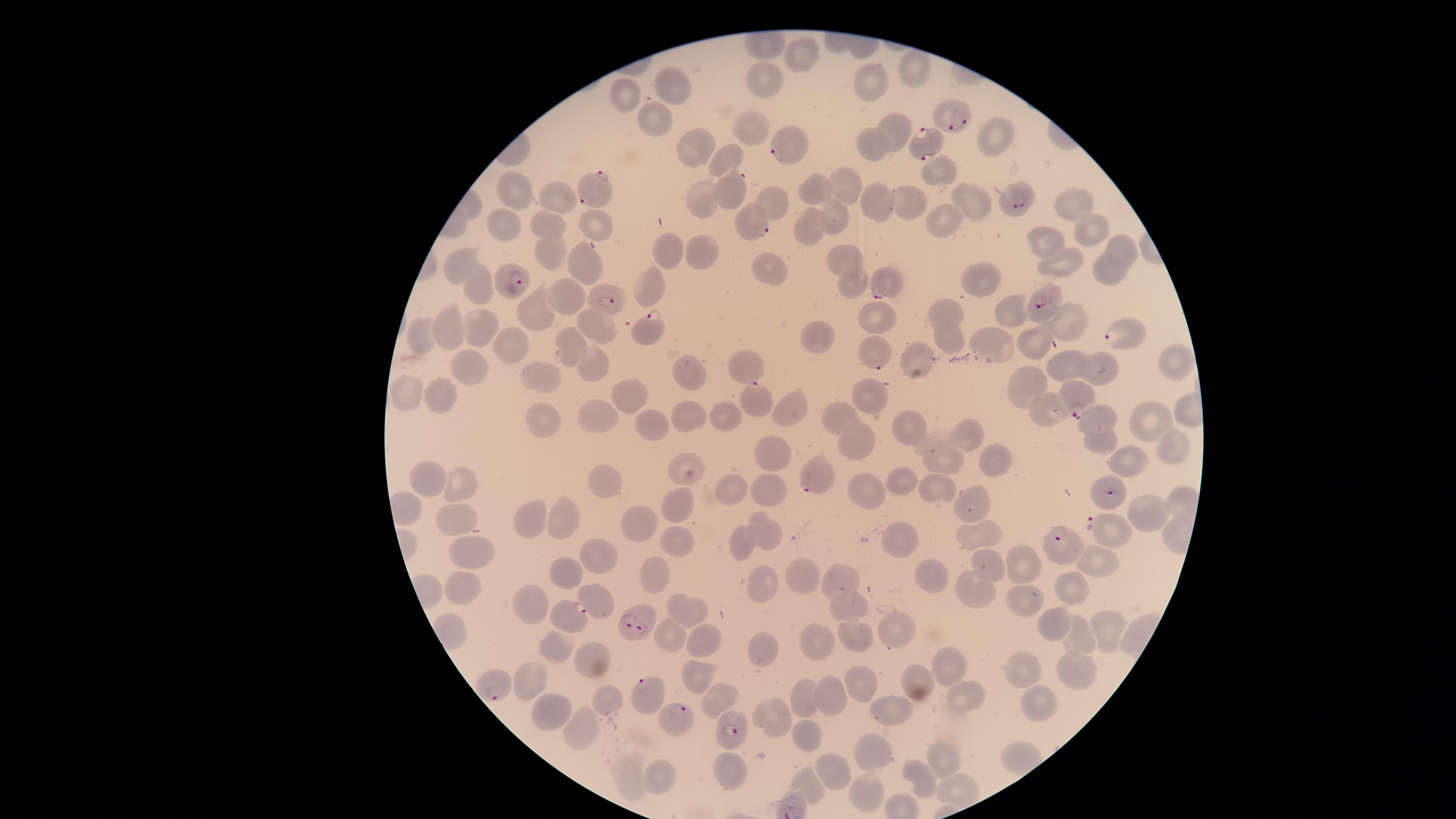
image_size: 1456×819 pixels
parasitized_RBCs: 'approximate marker points as (x, y) in pixels: (953, 122), (925, 144), (785, 148), (594, 190), (1019, 203), (756, 221), (517, 278), (886, 286), (606, 296), (1043, 306), (651, 328), (1120, 337), (877, 355), (755, 397), (1075, 398), (819, 476), (1114, 493), (1096, 525), (1061, 541), (570, 616), (642, 616), (487, 687), (644, 693), (679, 719), (728, 733)'
field_of_view: single
visible_region: circular
species: Plasmodium falciparum
stain: Giemsa
capture: smartphone photograph through the microscope eyepiece
presence: malaria parasites identified
uninfected_RBCs: 'approximate marker points as (x, y) in pixels: (805, 59), (910, 69), (873, 81), (764, 85), (673, 89), (620, 91), (650, 119), (749, 129), (894, 131), (997, 134), (872, 145), (691, 149), (730, 157), (938, 168), (843, 185), (518, 192), (817, 193), (732, 194), (557, 196), (1072, 199), (773, 200), (974, 200), (701, 201), (907, 202), (879, 207), (940, 216), (829, 218), (505, 224), (596, 224), (547, 226), (808, 228), (1082, 231), (1050, 238), (1118, 247), (697, 251), (666, 252), (553, 253), (841, 260), (585, 265), (463, 266), (1062, 267), (1112, 269), (776, 270), (976, 281), (855, 285), (478, 287), (652, 288), (571, 296), (944, 308), (1006, 310), (536, 311), (880, 320), (1069, 322), (478, 328), (440, 331), (593, 331), (820, 335), (947, 336), (421, 338), (1031, 339), (513, 343), (993, 344), (566, 346), (1171, 359), (917, 360), (749, 362), (591, 365), (1067, 365), (1101, 368), (696, 369), (466, 370), (542, 377), (1029, 383), (440, 394), (870, 394), (404, 395), (629, 398), (1048, 408), (791, 410), (723, 411), (1101, 411), (688, 412), (601, 415), (544, 417), (1143, 417), (841, 419), (659, 428), (912, 429), (851, 437), (967, 437), (932, 442), (1099, 445), (1172, 448), (773, 454), (943, 459), (1132, 460), (999, 462), (688, 470), (601, 481), (431, 482), (906, 482), (769, 484), (869, 484), (458, 487), (725, 490), (940, 491), (681, 503), (974, 503), (1139, 513), (458, 514), (526, 515), (565, 515), (638, 521), (766, 531), (974, 531), (899, 536), (674, 538), (741, 541), (466, 547), (1092, 557), (599, 559), (989, 562), (1023, 563), (650, 567), (564, 571), (794, 575), (839, 578), (939, 578), (756, 579), (978, 583), (455, 584), (1073, 590), (1022, 598), (595, 599), (530, 602), (843, 606), (691, 610), (1059, 626), (1109, 627), (897, 629), (851, 633), (1084, 634), (672, 638), (707, 641), (822, 643), (767, 645), (549, 649), (591, 662), (947, 665), (1070, 666), (1025, 668), (697, 671), (533, 679), (918, 680), (856, 685), (719, 695), (810, 696), (831, 696), (611, 697), (973, 697), (1038, 704), (895, 708), (556, 713), (773, 715), (583, 730), (800, 738), (877, 753), (946, 765), (732, 772), (831, 772), (660, 774), (922, 777), (631, 780), (809, 786), (868, 789), (958, 791)'
preparation: thin smear of blood